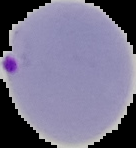

From a thin blood film. The area outside the segmented cell region is set to black. Result: Plasmodium parasites identified. Image is 136×148 pixels.